Identify the preparation type.
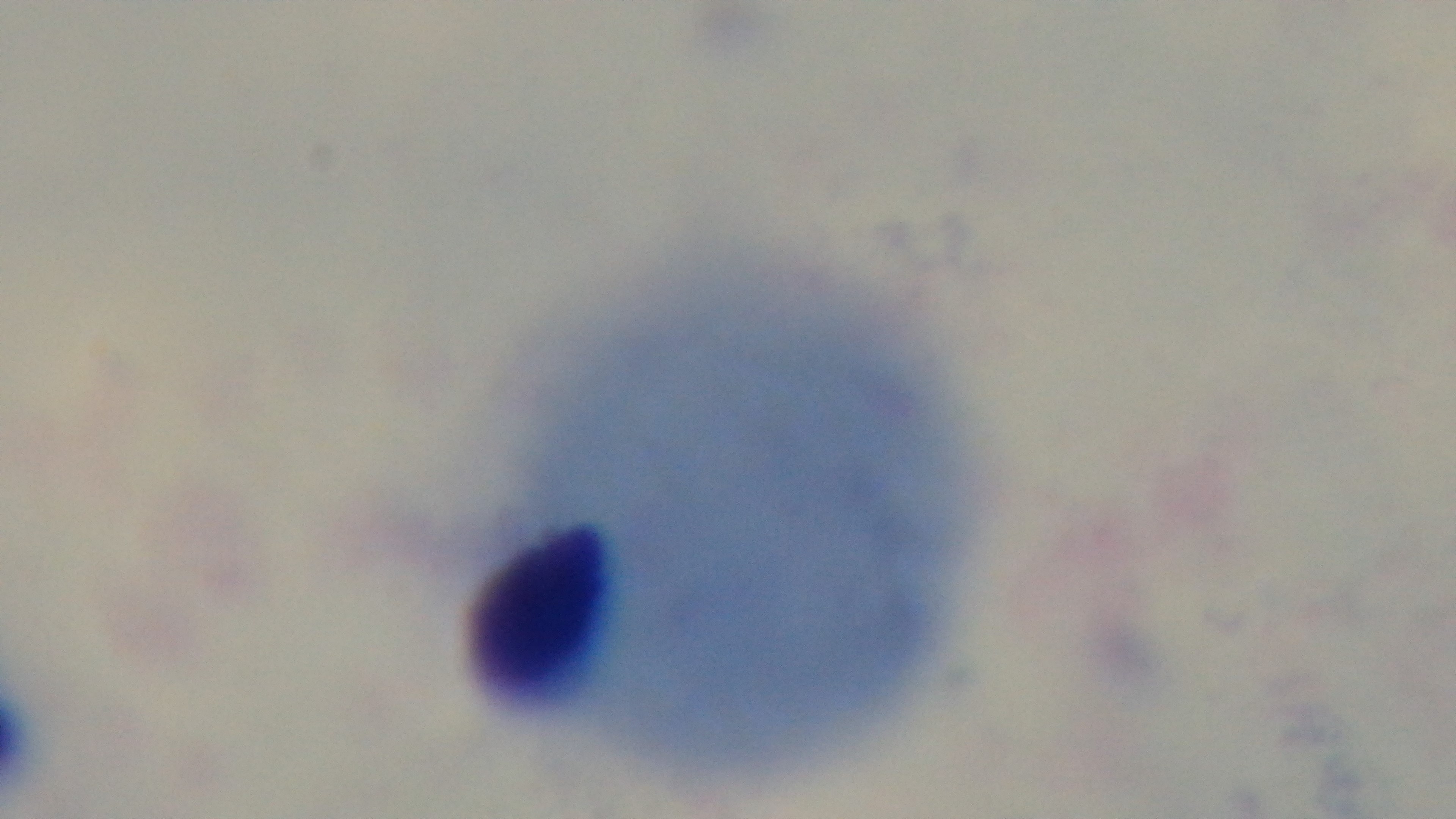

A thick smear.

Summary:
  - Modality: light microscopy
  - Objective: 100x oil immersion
  - Capture: mounted 4K digital camera
  - Malaria status: negative
  - Stain: Giemsa
  - Field of view: one from the slide